Name the parasite shown.
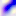
This is Toxoplasma gondii.

modality: micrograph
magnification: 400x